Locate and identify every blood parasite.
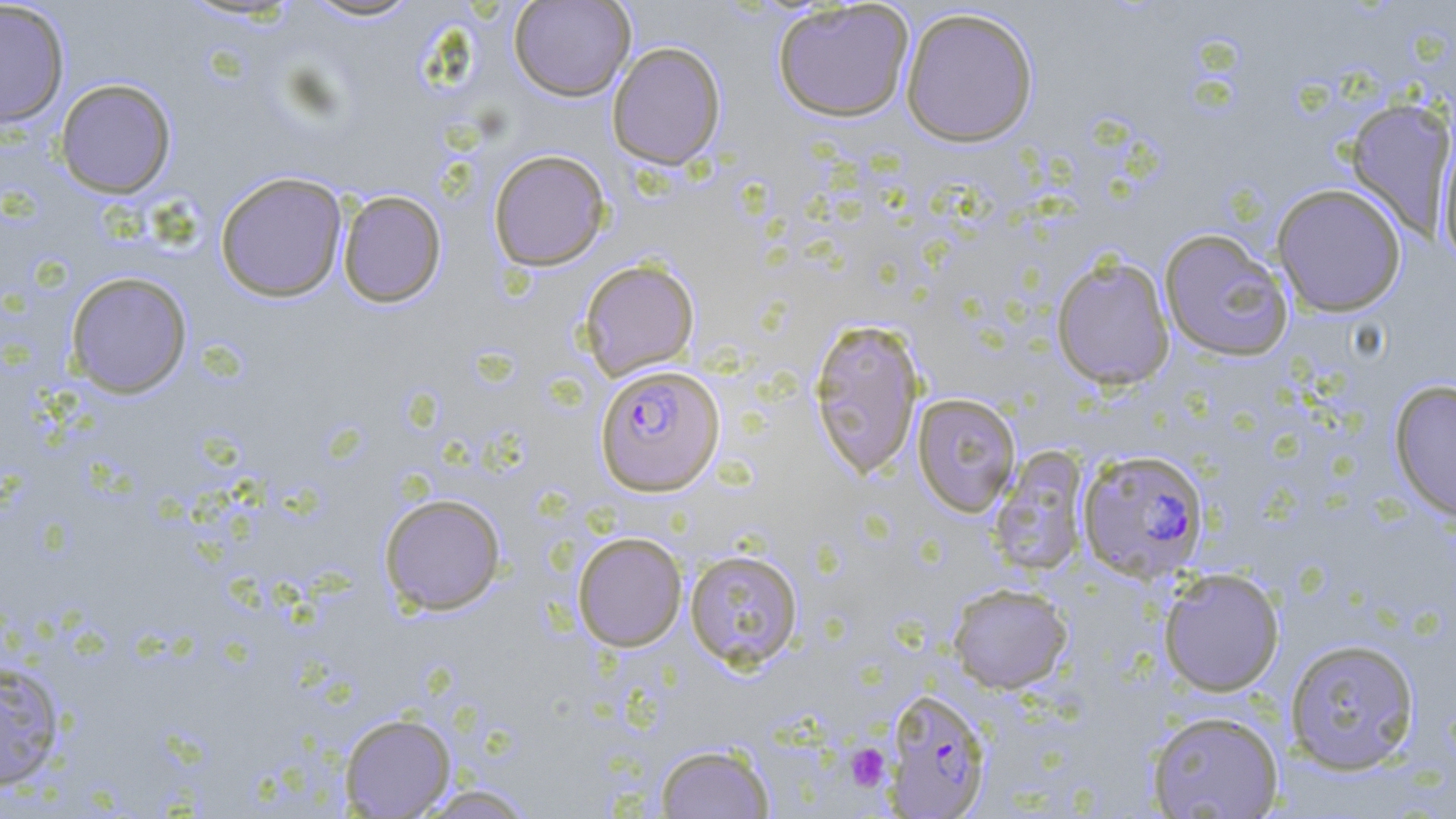

Approximate bounding boxes as (x1, y1, x2, y2) in pixels.
Plasmodium falciparum-infected red blood cells: (595, 364, 725, 496), (1077, 448, 1210, 583), (884, 688, 993, 817).
No Plasmodium ovale, Plasmodium malariae, Plasmodium vivax, Babesia divergens, or Trypanosoma brucei observed.

slide-level diagnosis = Plasmodium falciparum
field of view = single
stain = May-Grünwald-Giemsa
modality = light microscopy
platelet locations = approximate bounding boxes as (x1, y1, x2, y2) in pixels: (846, 744, 890, 790)
preparation = thin blood film
uninfected red blood cell locations = approximate bounding boxes as (x1, y1, x2, y2) in pixels: (300, 0, 424, 23), (508, 0, 636, 102), (0, 1, 70, 130), (772, 2, 915, 122), (899, 6, 1039, 147), (607, 41, 726, 170), (54, 78, 177, 198), (1345, 97, 1456, 239), (1434, 129, 1456, 266), (488, 149, 611, 272), (214, 171, 348, 302), (1271, 183, 1407, 317), (337, 189, 447, 308), (1159, 229, 1293, 362), (1051, 254, 1176, 391), (579, 259, 700, 381), (65, 271, 193, 398), (808, 318, 925, 480), (1388, 379, 1456, 522), (912, 393, 1021, 517), (987, 446, 1090, 577), (379, 493, 507, 615), (572, 531, 688, 651), (684, 548, 803, 671), (1158, 567, 1285, 697), (947, 583, 1074, 694), (1284, 637, 1421, 775), (0, 662, 67, 791), (1145, 709, 1285, 818), (339, 712, 456, 817), (654, 743, 774, 818), (411, 784, 539, 818)
image size = 1456×819 pixels
magnification = 1000x